Comment on the morphology of the red blood cells.
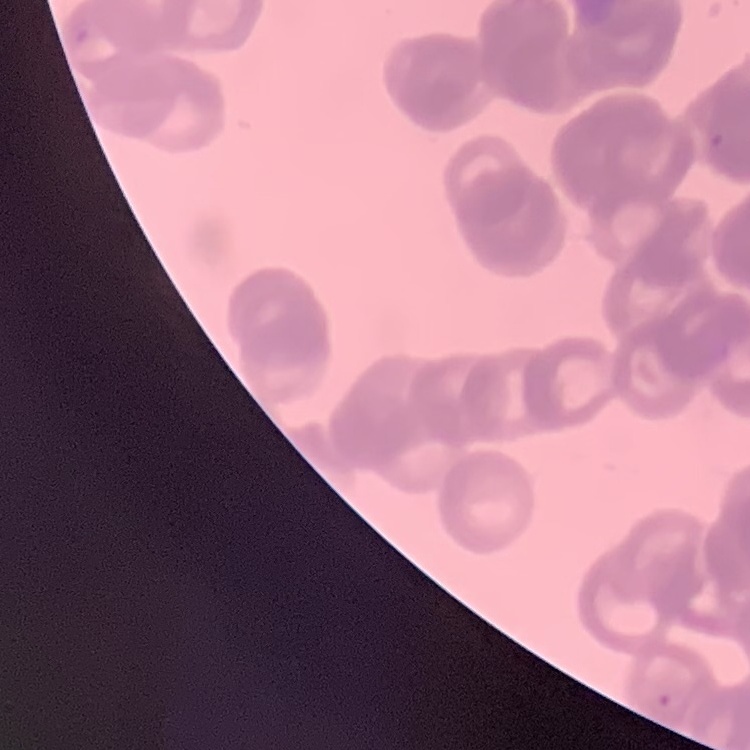

Rouleaux formation.

Thin blood smear. Stained with either Field's or Giemsa. One tile cut from a larger photomicrograph.